Assess this cell for malaria.
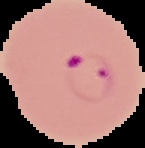

It is parasitized.

image size = 145×148 pixels
image type = segmented cell region with the area outside set to black
preparation = thin blood smear